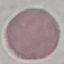
{
  "malaria_status": "uninfected",
  "stain": "Giemsa",
  "capture": "smartphone camera at the microscope eyepiece",
  "preparation": "thin blood smear",
  "image_type": "cell patch, automatically extracted from a larger field of view and resized to 64 × 64 pixels"
}